Assess this cell for malaria.
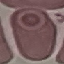

Uninfected.

Cell patch, automatically extracted from a larger field of view and resized to 64 × 64 pixels. Photographed with a smartphone camera at the microscope eyepiece. Giemsa-stained preparation. Thin smear of blood.